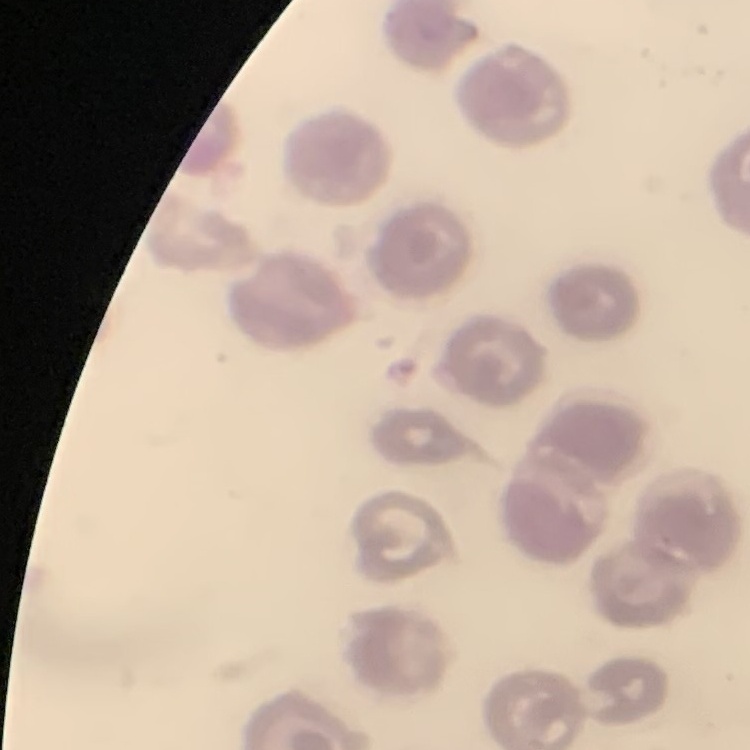 The erythrocytes exhibit no rouleaux formation. Thin blood smear. Field's or Giemsa stain. One tile cut from a larger photomicrograph.